Name the blood parasite species.
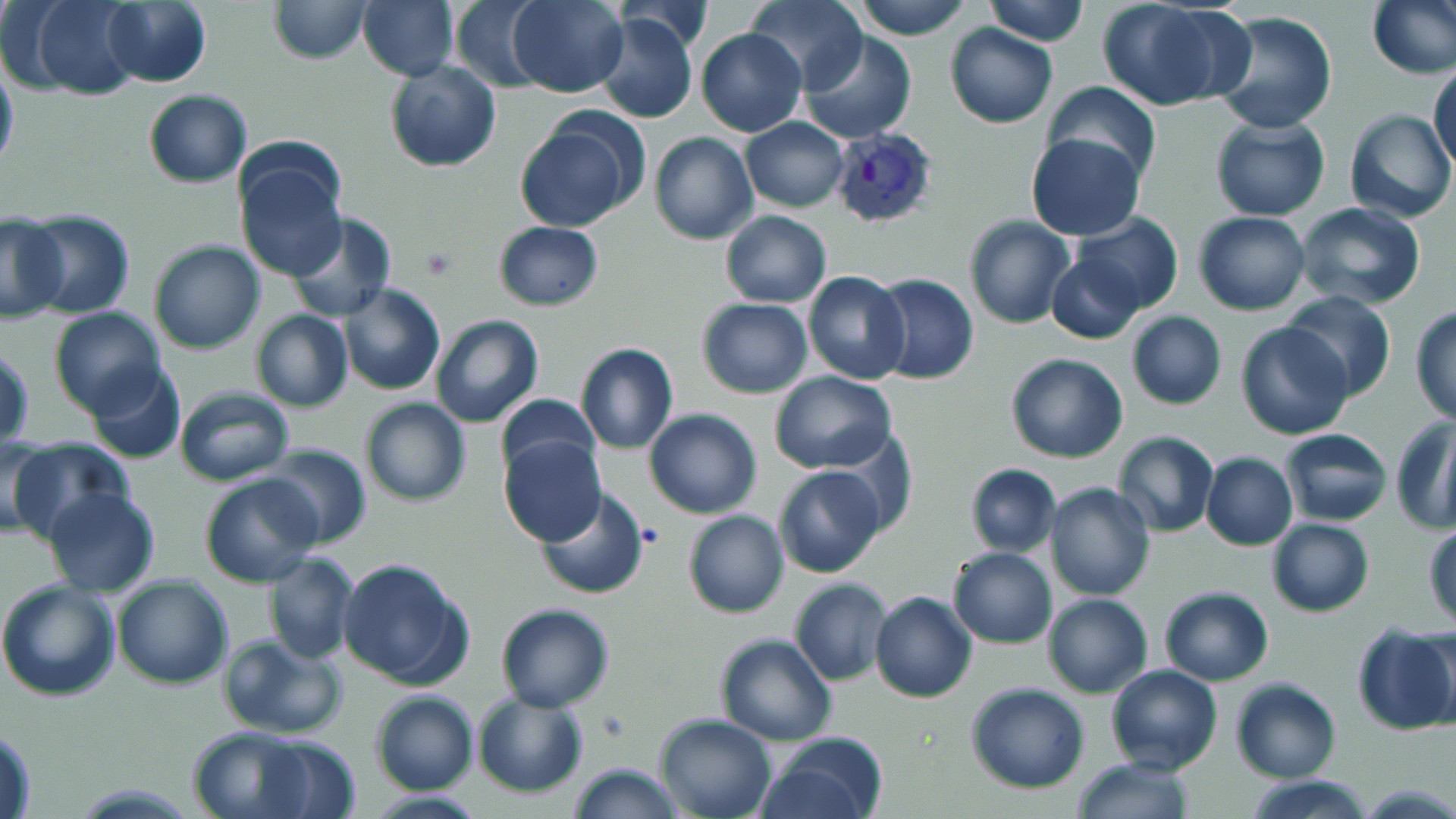
Plasmodium vivax.

magnification = 1000x
platelet locations = approximate bounding boxes as (x1, y1, x2, y2) in pixels: (418, 246, 458, 283), (595, 709, 631, 739)
modality = light microscopy
preparation = thin blood smear
stain = May-Grünwald-Giemsa
image size = 1456×819 pixels
Plasmodium vivax-infected red blood cell locations = approximate bounding boxes as (x1, y1, x2, y2) in pixels: (828, 126, 941, 228)
field of view = single
uninfected red blood cell locations = approximate bounding boxes as (x1, y1, x2, y2) in pixels: (19, 0, 146, 101), (269, 0, 373, 64), (357, 0, 459, 82), (505, 0, 629, 98), (745, 0, 869, 93), (853, 0, 973, 40), (984, 0, 1087, 46), (1369, 0, 1455, 79), (447, 1, 549, 92), (1097, 1, 1227, 111), (102, 2, 211, 87), (593, 11, 700, 125), (1210, 11, 1338, 134), (944, 23, 1057, 129), (695, 27, 807, 139), (798, 34, 919, 145), (0, 52, 19, 178), (384, 60, 501, 173), (1431, 61, 1456, 176), (1043, 82, 1161, 185), (143, 89, 252, 188), (1343, 110, 1454, 224), (513, 115, 645, 232), (740, 116, 849, 212), (1208, 117, 1330, 221), (649, 131, 758, 245), (1026, 132, 1145, 240), (234, 148, 347, 283), (1294, 202, 1425, 311), (22, 210, 136, 318), (719, 211, 832, 307), (1192, 211, 1310, 315), (1074, 212, 1185, 314), (286, 213, 398, 322), (964, 214, 1075, 329), (0, 216, 68, 324), (493, 219, 603, 311), (149, 240, 266, 354), (1046, 252, 1144, 345), (803, 271, 911, 386), (871, 273, 979, 384), (337, 284, 446, 398), (1281, 291, 1397, 401), (697, 298, 814, 399), (1411, 305, 1456, 426), (49, 307, 167, 419), (252, 311, 353, 411), (1125, 312, 1227, 410), (428, 315, 543, 428), (1236, 320, 1356, 439), (576, 342, 678, 454), (1, 346, 35, 453), (1004, 352, 1129, 462), (86, 364, 188, 465), (769, 370, 896, 474), (173, 386, 294, 486), (496, 394, 601, 483), (360, 398, 471, 506), (644, 409, 761, 518), (1392, 414, 1456, 533), (1278, 428, 1393, 526), (1114, 431, 1219, 539), (0, 433, 54, 539), (498, 436, 604, 546), (5, 438, 133, 548), (259, 444, 371, 548), (1200, 452, 1298, 551), (965, 464, 1060, 557), (773, 465, 886, 579), (200, 475, 324, 588), (1044, 483, 1155, 601), (44, 487, 160, 598), (532, 487, 651, 601), (683, 508, 789, 618), (1266, 518, 1376, 617), (1424, 524, 1456, 630), (946, 546, 1057, 647), (261, 552, 359, 665), (337, 556, 474, 690), (113, 574, 233, 691), (790, 577, 893, 686), (0, 580, 122, 701), (1158, 586, 1274, 685), (870, 591, 977, 704), (1043, 592, 1152, 697), (496, 603, 613, 711), (1354, 623, 1456, 737), (219, 633, 347, 739), (715, 633, 837, 745), (1104, 664, 1224, 775), (1230, 678, 1340, 782), (967, 682, 1091, 794), (369, 690, 479, 796), (472, 693, 589, 797), (654, 713, 778, 819), (1, 725, 38, 817), (188, 726, 334, 818), (255, 733, 359, 819), (758, 733, 887, 819), (1069, 756, 1196, 818), (567, 761, 684, 818), (1247, 773, 1375, 819)